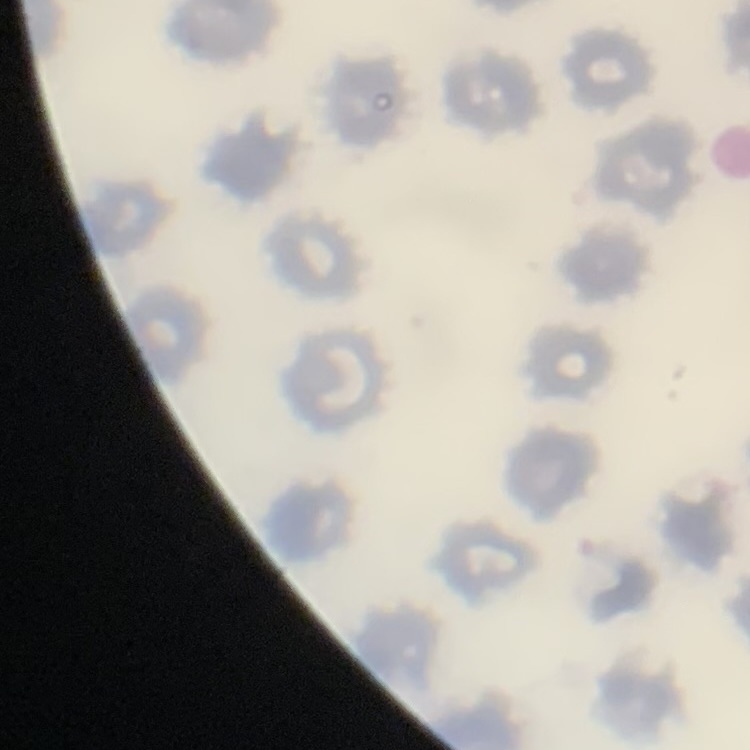

Summary:
  - Erythrocyte morphology: no rouleaux formation
  - Stain: Field's or Giemsa
  - Image type: one tile cut from a larger photomicrograph
  - Preparation: thin blood smear